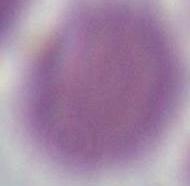
1000x magnification. An erythrocyte is shown. Micrograph.